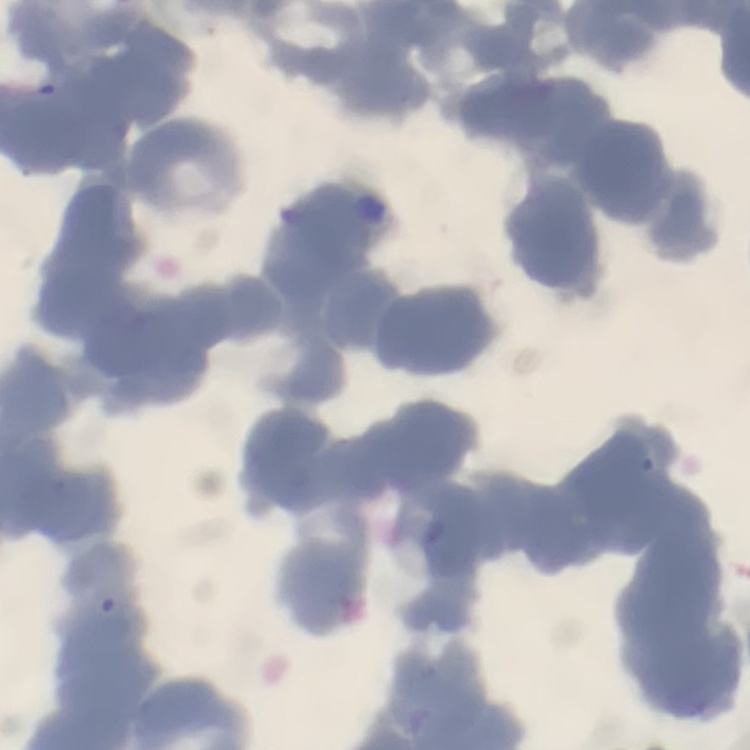 The red blood cells show rouleaux formation. Thin peripheral smear. One tile cut from a larger photomicrograph. Field's or Giemsa stain.